Identify the parasite.
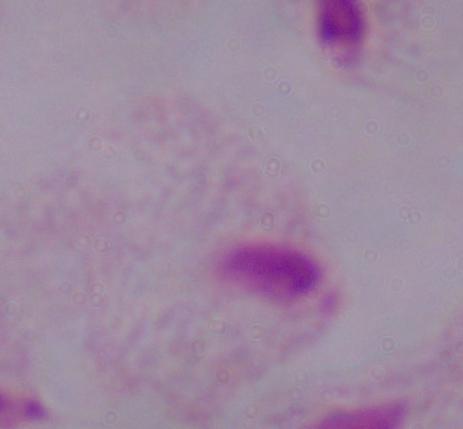
A trichomonad.

Summary:
  - Modality: micrograph
  - Magnification: 1000x